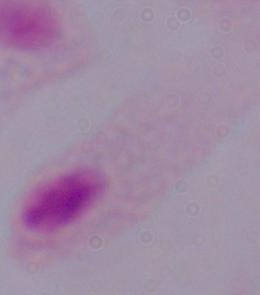

Captured at 1000x magnification. A trichomonad is shown. Micrograph.